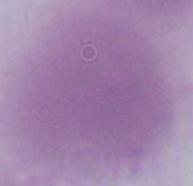 Micrograph. 1000x magnification. A red blood cell is shown.